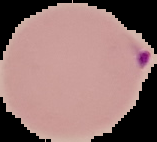

Summary:
  - Preparation: thin blood smear
  - Malaria status: parasitized
  - Image size: 157×142 pixels
  - Image type: cell region segmented out of the field of view; surrounding area masked to black